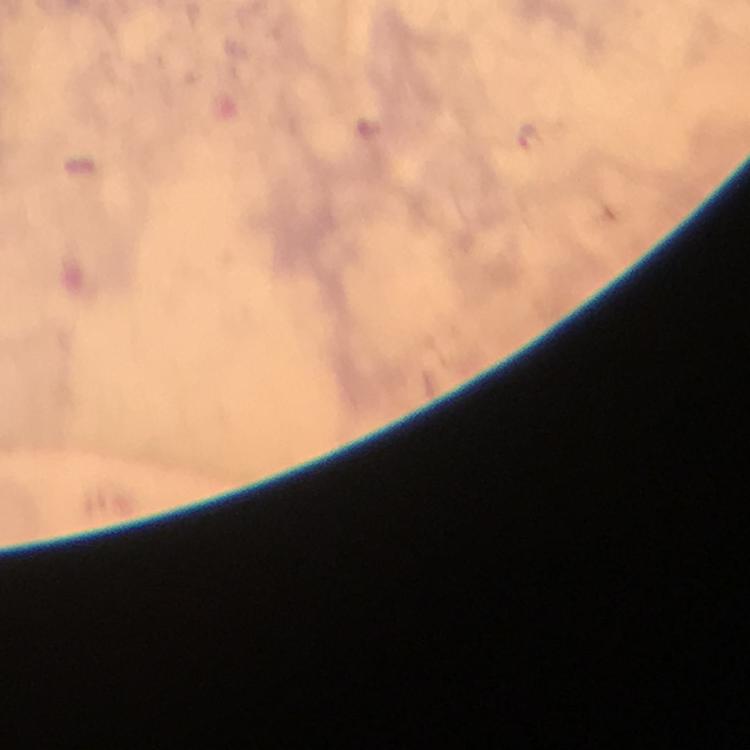 Approximate centers as (x, y) in pixels. Plasmodium parasite locations: (531, 138). Thick smear. Photographed with a smartphone mounted on the microscope. Cropped region of a single field of view. Image is 750×750 pixels. Giemsa stain. Immersion oil applied. At 100x magnification. From a malaria diagnostic workup.